Comment on the morphology of the red blood cells.
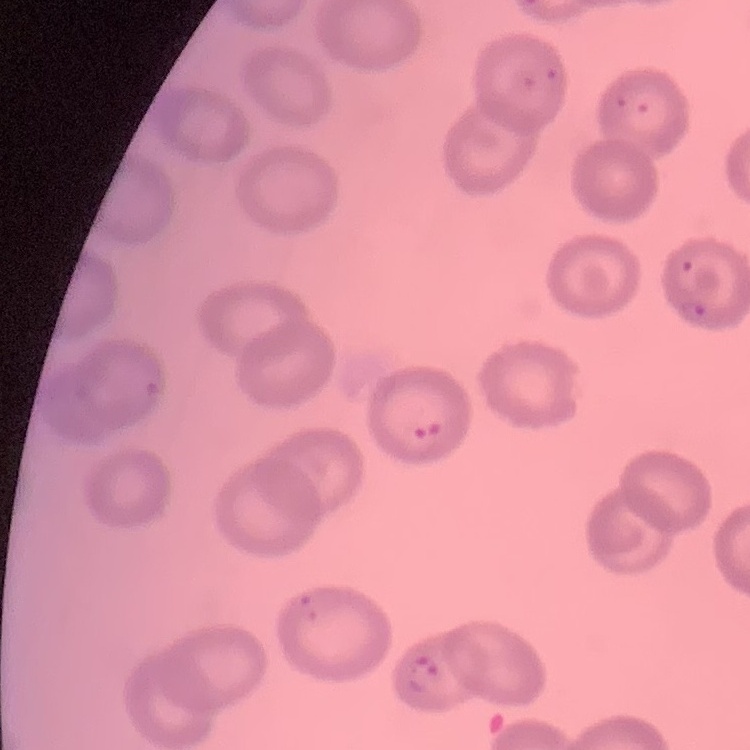
They show no rouleaux formation.

image type = square crop of a larger photomicrograph
preparation = thin peripheral smear
stain = Field's or Giemsa